Give the position of every malaria parasite.
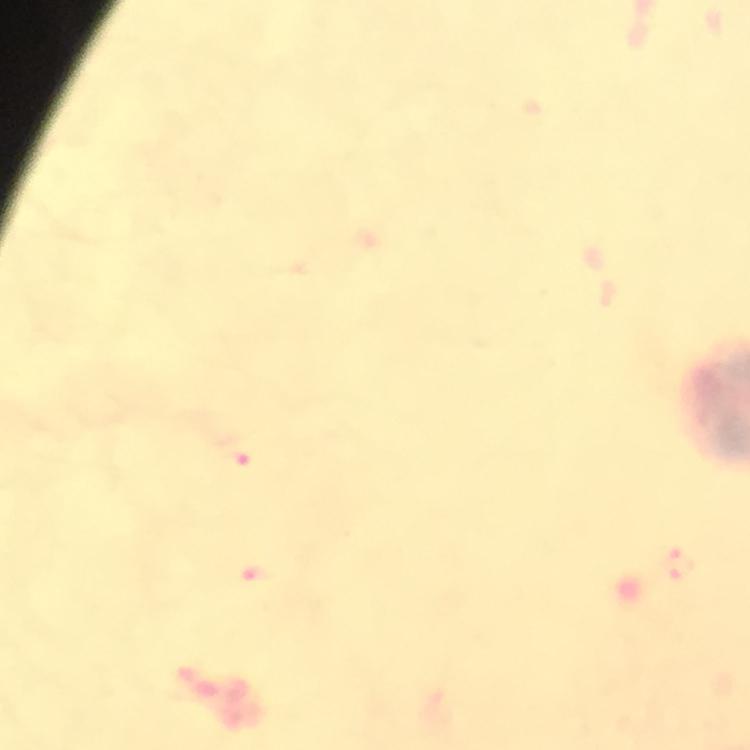

Approximate centers as [x, y] in pixels.
Malaria parasites: [237, 451], [680, 563], [262, 579].

context = from a malaria diagnostic workup
stain = Giemsa
preparation = thick smear
magnification = 100x
immersion oil = used
capture = smartphone camera through the microscope
cropped from = one field of view
image size = 750×750 pixels